Describe the morphology of the red blood cells.
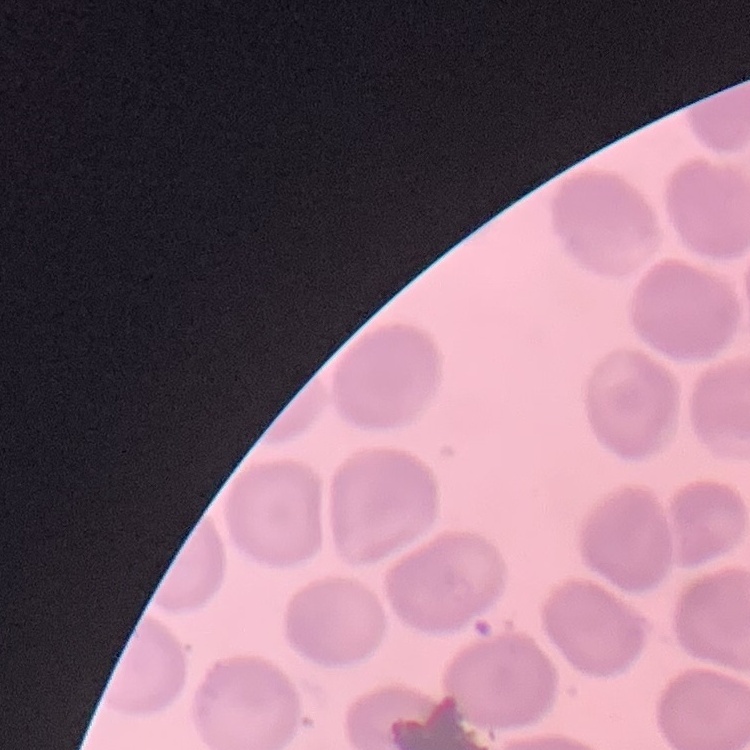
No rouleaux formation.

{
  "preparation": "thin peripheral smear",
  "stain": "Field's or Giemsa",
  "image_type": "square crop of a larger photomicrograph"
}